Outline every malaria parasite.
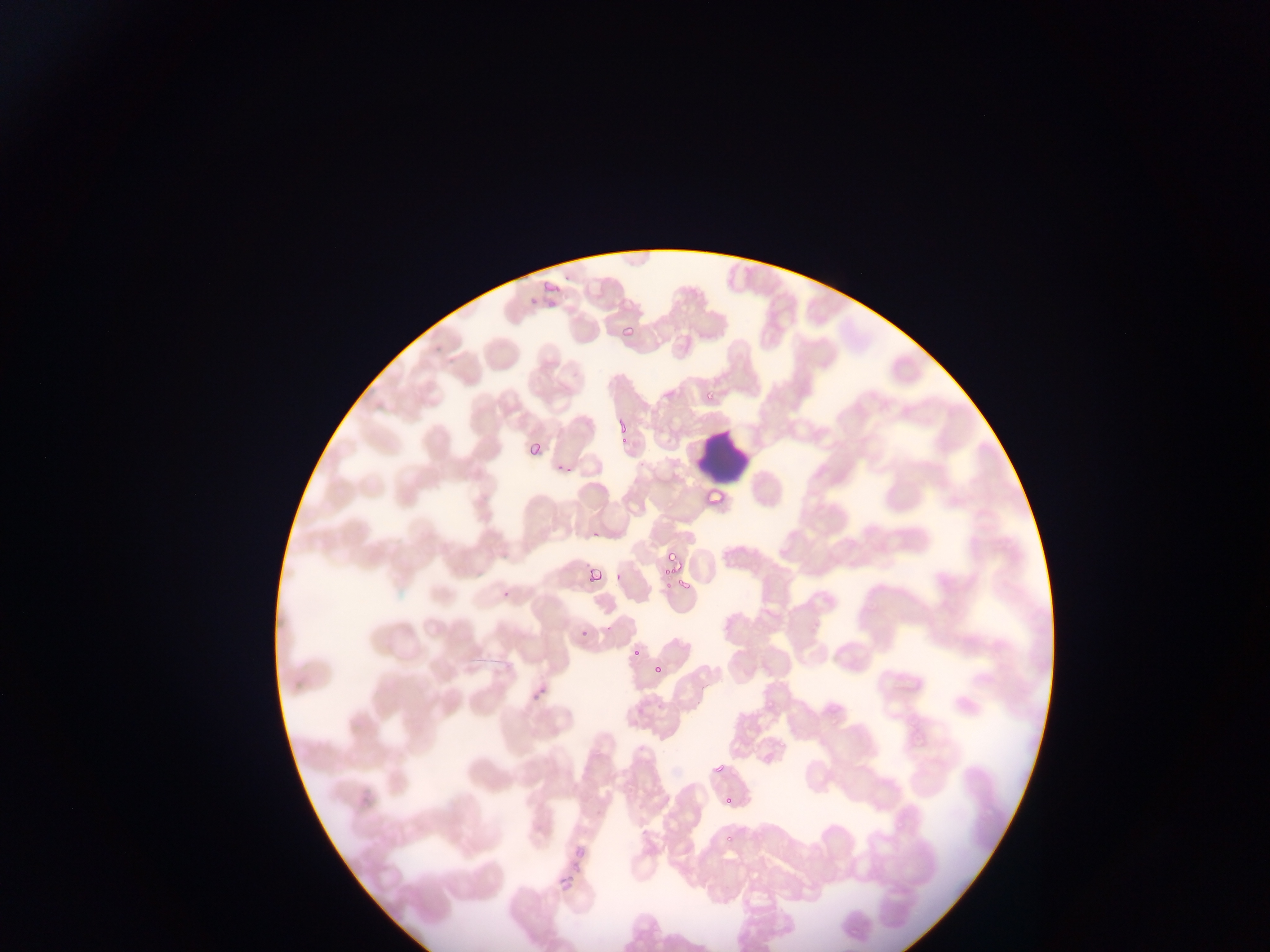

Approximate bounding boxes as {left, top, right, bottom} in pixels.
Malaria parasites: {534, 281, 560, 305}, {619, 323, 635, 340}, {707, 388, 719, 403}, {613, 416, 630, 433}, {525, 436, 544, 455}, {617, 436, 628, 447}, {554, 462, 575, 472}, {705, 487, 725, 508}, {592, 529, 603, 540}, {664, 550, 679, 566}, {585, 567, 602, 583}, {663, 571, 678, 589}, {613, 572, 625, 583}, {678, 577, 692, 592}, {498, 584, 516, 598}, {579, 625, 590, 637}, {631, 647, 642, 658}, {649, 660, 664, 677}, {531, 686, 546, 702}, {711, 760, 727, 776}, {721, 794, 734, 808}, {724, 835, 734, 844}, {563, 843, 592, 876}, {555, 855, 586, 888}, {556, 868, 578, 891}.

Leukocyte locations: {694, 435, 750, 482}. Collected in Ghana. Image is 1270×952 pixels. Mobile-phone photograph taken through the microscope. Thin blood film. One field of view.